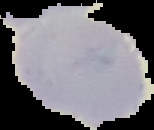 Cell region segmented out of the field of view; the surrounding area is masked to black. Image is 154×130 pixels. From a thin blood film. Malaria status: uninfected.